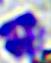

identification = white blood cell
modality = micrograph
magnification = 400x